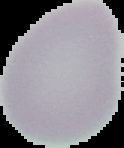 Malaria status: uninfected. From a thin blood smear. Cell region segmented out of the field of view; the surrounding area is masked to black. Image is 124×148 pixels.